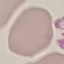
Summary:
  - Result: no malaria parasites detected
  - Capture: smartphone camera at the microscope eyepiece
  - Image type: cell patch, automatically extracted from a larger field of view and resized to 64 × 64 pixels
  - Preparation: thin blood smear
  - Stain: Giemsa